Assess for malaria.
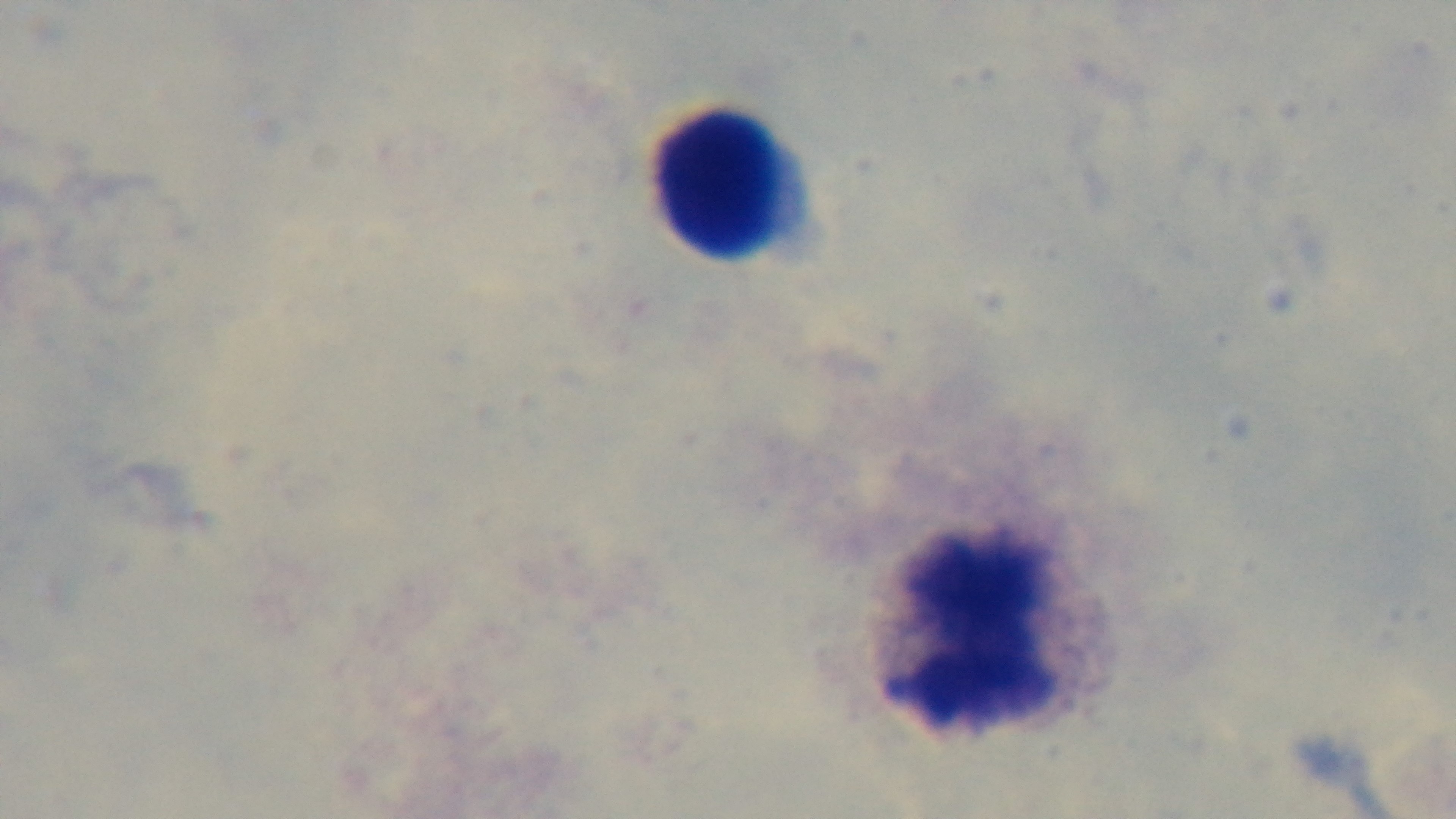

Negative.

Light microscopy. Giemsa-stained. 100x oil-immersion objective. One field from the slide. Captured with a mounted 4K digital camera. Preparation: thick smear.